Report the malaria status of this cell.
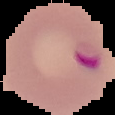

Parasitized.

{
  "preparation": "thin blood smear",
  "image_type": "segmented cell region on a black background",
  "image_size": "115×115 pixels"
}